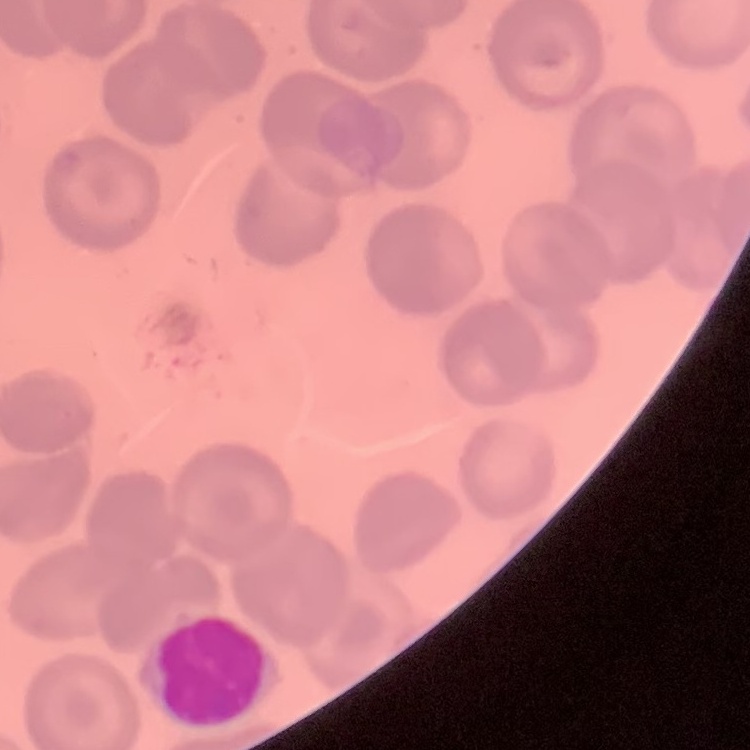

erythrocyte morphology = no rouleaux formation
preparation = thin peripheral smear
image type = square crop of a larger photomicrograph
stain = Field's or Giemsa